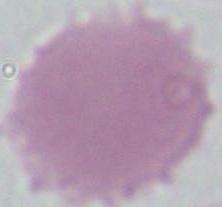 Micrograph. An erythrocyte is seen. 1000x magnification.